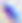

identification: Toxoplasma gondii
magnification: 400x
modality: photomicrograph